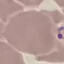
malaria status = parasitized
stain = Giemsa
capture = smartphone through the microscope eyepiece
image type = cell patch, automatically extracted from a larger field of view and resized to 64 × 64 pixels
preparation = thin blood smear